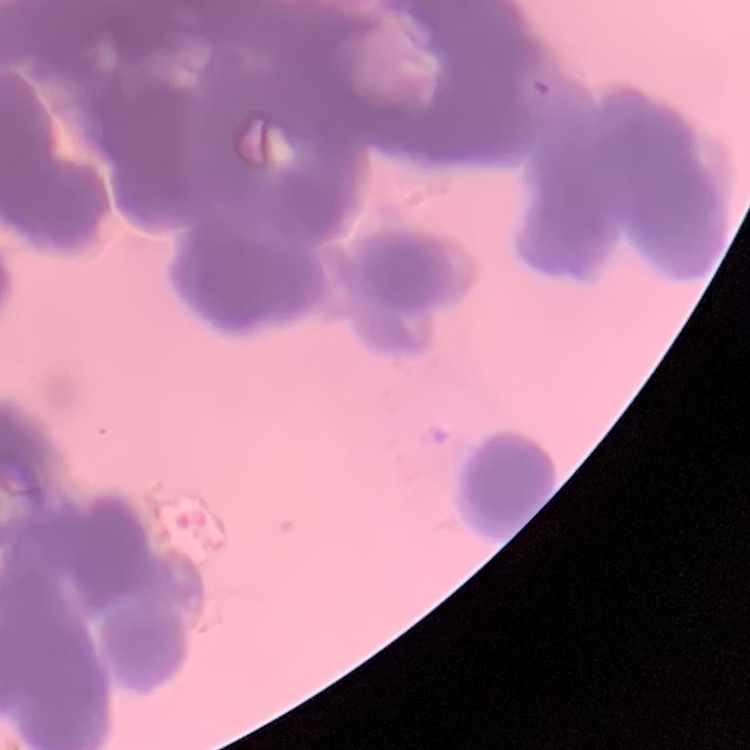 The erythrocytes show rouleaux formation. Square crop of a larger photomicrograph. Field's or Giemsa stain. Thin blood smear.